State the blood parasite species.
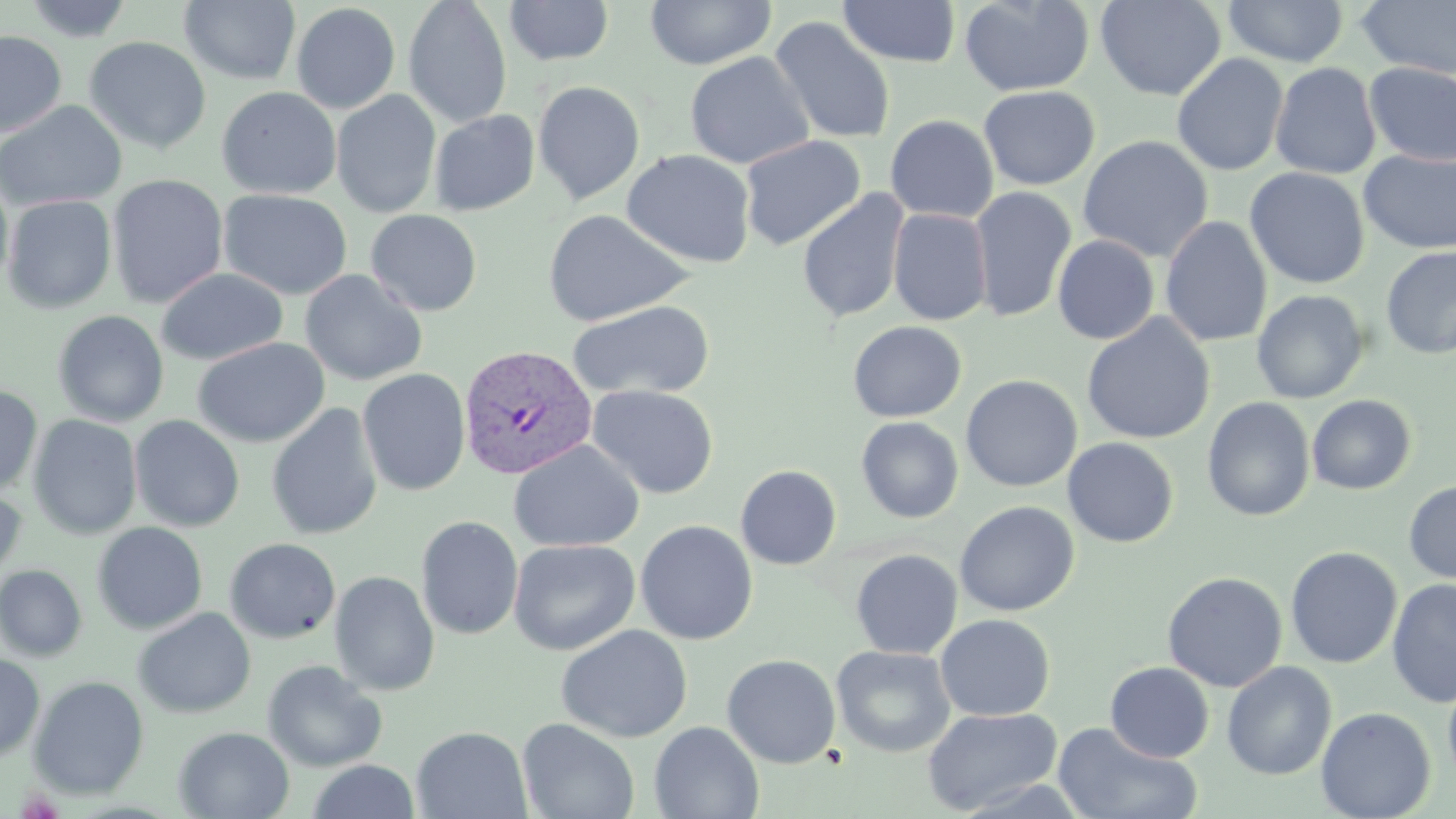

Plasmodium vivax.

Approximate bounding boxes as [x1, y1, x2, y2] in pixels. Plasmodium vivax-infected red blood cell locations: [458, 345, 598, 480]. Uninfected red blood cell locations: [23, 0, 134, 42], [403, 0, 513, 128], [645, 0, 776, 70], [958, 0, 1095, 96], [1095, 0, 1226, 101], [1223, 0, 1349, 67], [179, 1, 301, 85], [504, 1, 614, 66], [837, 1, 962, 68], [1356, 1, 1456, 79], [291, 3, 401, 114], [768, 15, 897, 146], [0, 30, 66, 137], [84, 36, 211, 154], [684, 52, 814, 169], [1171, 53, 1289, 176], [1270, 62, 1382, 179], [1364, 63, 1456, 166], [533, 80, 645, 205], [979, 85, 1100, 190], [216, 86, 341, 199], [331, 89, 442, 218], [0, 100, 127, 213], [429, 109, 540, 216], [885, 114, 999, 223], [740, 134, 866, 251], [1077, 135, 1214, 263], [621, 149, 756, 268], [1359, 149, 1456, 255], [1245, 167, 1369, 289], [0, 171, 14, 293], [107, 174, 228, 309], [970, 187, 1076, 324], [217, 188, 353, 301], [797, 189, 910, 324], [2, 194, 117, 314], [888, 208, 993, 325], [366, 209, 483, 316], [542, 209, 695, 326], [1159, 216, 1272, 347], [1052, 235, 1160, 345], [1381, 246, 1456, 359], [156, 267, 288, 366], [299, 269, 428, 386], [1251, 289, 1370, 404], [567, 300, 716, 400], [52, 310, 169, 427], [1081, 314, 1216, 445], [847, 320, 966, 422], [192, 337, 330, 447], [357, 368, 471, 495], [961, 374, 1083, 492], [587, 384, 720, 499], [0, 385, 42, 497], [1307, 394, 1417, 495], [1202, 396, 1316, 522], [266, 402, 383, 541], [28, 414, 142, 539], [129, 415, 245, 532], [856, 416, 963, 523], [508, 438, 645, 553], [1062, 438, 1179, 547], [735, 464, 841, 570], [1403, 479, 1456, 584], [0, 487, 27, 590], [955, 500, 1079, 616], [415, 515, 523, 640], [635, 520, 758, 645], [92, 522, 208, 635], [224, 537, 341, 644], [508, 538, 640, 656], [1284, 546, 1403, 669], [851, 549, 962, 659], [0, 564, 87, 662], [329, 570, 440, 696], [1162, 571, 1288, 692], [1386, 578, 1456, 708], [132, 607, 257, 719], [935, 613, 1055, 721], [555, 624, 693, 743], [831, 645, 956, 758], [0, 652, 45, 763], [721, 654, 841, 768], [262, 660, 387, 772], [1105, 661, 1214, 763], [1222, 661, 1337, 780], [1442, 670, 1456, 787], [28, 675, 149, 800], [922, 706, 1064, 815], [1316, 706, 1437, 819], [517, 718, 640, 819], [649, 721, 763, 819], [1054, 722, 1201, 819], [173, 726, 294, 818], [411, 726, 532, 818], [306, 759, 421, 818]. May-Grünwald-Giemsa-stained preparation. Optical microscopy. Image is 1456×819 pixels. Single field of view. 1000x magnification. Thin blood film.